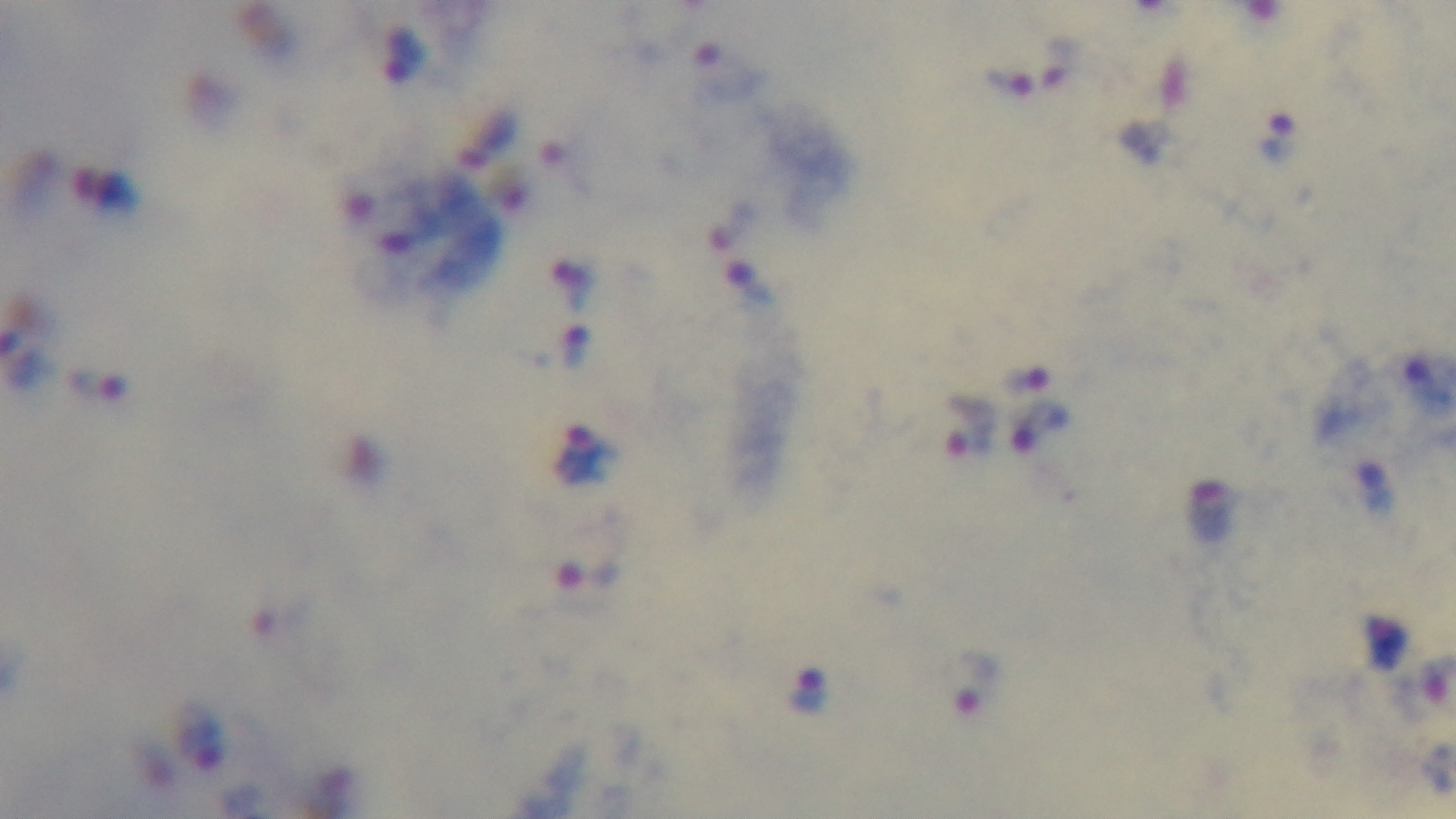

Summary:
  - Capture: mounted 4K digital camera
  - Objective: 100x oil immersion
  - Malaria status: positive
  - Modality: light microscopy
  - Field of view: one from the slide
  - Stain: Giemsa
  - Preparation: thick smear